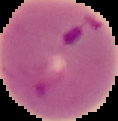
preparation: thin blood smear
result: Plasmodium parasites detected
image_size: 118×121 pixels
image_type: segmented cell region on a black background